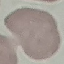
result: no malaria parasites detected
capture: smartphone camera at the microscope eyepiece
preparation: thin blood smear
stain: Giemsa
image_type: automatically extracted cell patch, resized to 64 × 64 pixels